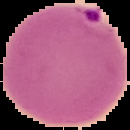
From a thin blood smear. Cell region segmented out of the field of view; the surrounding area is masked to black. Malaria status: parasitized. Image is 130×130 pixels.